Name the blood parasite species.
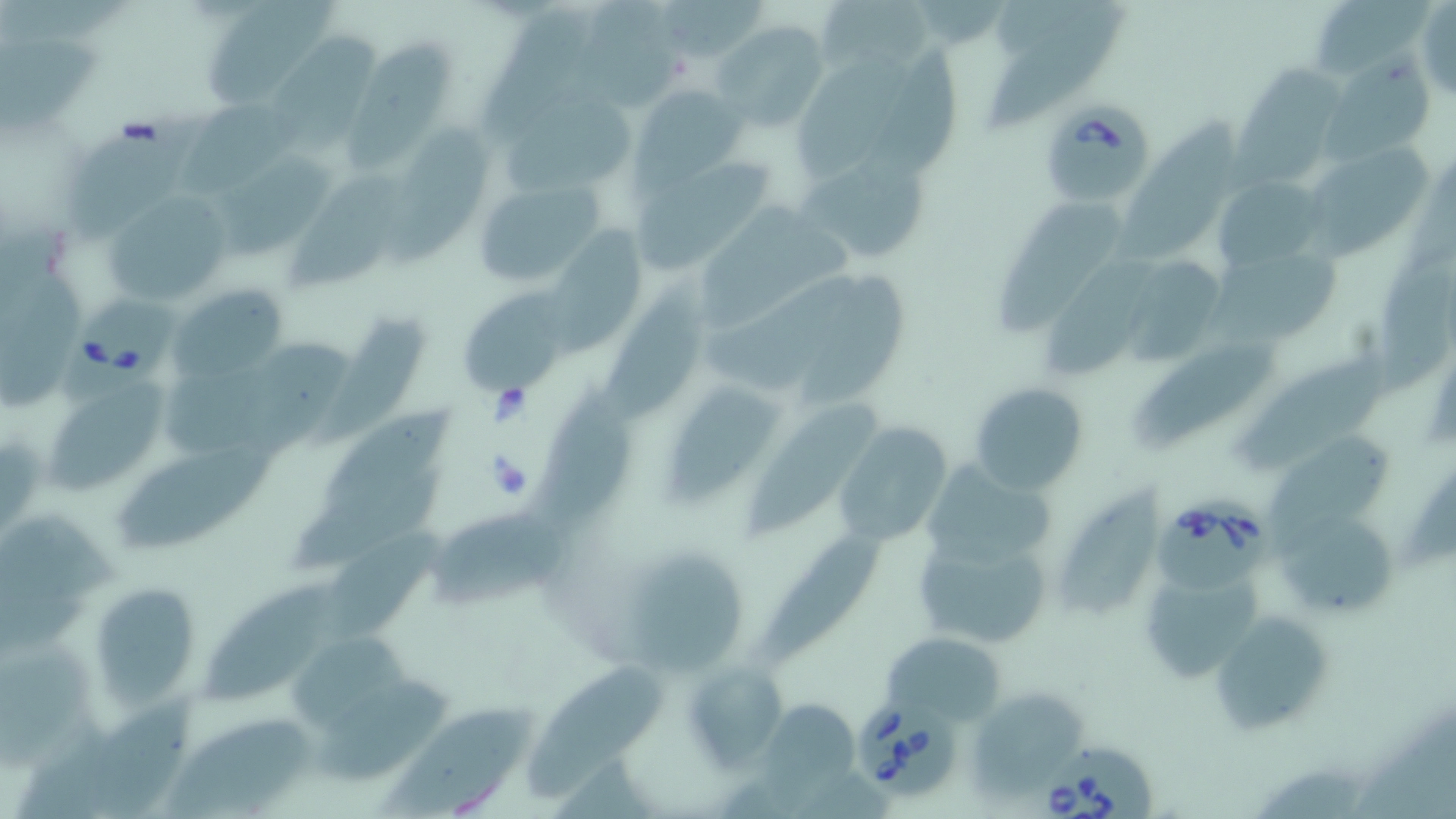
Babesia divergens.

Summary:
  - Coordinate format: approximate bounding boxes as (x1,y1)-(x2,y2) corner pairs in pixels
  - Uninfected red blood cell locations: (204,0)-(341,102), (659,0)-(764,65), (815,0)-(938,84), (914,0)-(999,43), (1314,0)-(1443,77), (575,1)-(689,110), (1415,4)-(1455,105), (478,5)-(597,144), (990,7)-(1129,131), (714,19)-(830,129), (265,27)-(380,158), (350,32)-(456,171), (3,33)-(102,131), (866,49)-(958,183), (795,55)-(919,184), (1319,56)-(1431,162), (1231,68)-(1351,200), (630,86)-(744,188), (506,87)-(632,197), (183,94)-(306,196), (66,106)-(203,240), (390,119)-(493,265), (1122,120)-(1241,265), (1307,142)-(1436,261), (204,146)-(339,260), (797,146)-(927,267), (635,154)-(778,272), (292,168)-(410,291), (1213,176)-(1326,276), (474,177)-(605,286), (1005,186)-(1133,331), (104,194)-(236,304), (695,198)-(858,333), (540,227)-(649,364), (1050,256)-(1152,383), (1379,256)-(1456,402), (1205,257)-(1344,354), (1132,262)-(1222,363), (1,270)-(80,408), (605,274)-(703,425), (804,275)-(914,409), (703,276)-(858,396), (169,278)-(288,384), (457,286)-(573,397), (313,302)-(438,456), (241,334)-(350,454), (1141,337)-(1279,452), (1252,347)-(1387,472), (166,360)-(289,458), (666,378)-(788,502), (49,379)-(178,494), (970,382)-(1089,495), (537,384)-(630,532), (751,402)-(892,536), (321,403)-(463,512), (836,420)-(952,546), (1268,435)-(1395,562), (112,439)-(274,548), (921,462)-(1059,573), (294,476)-(442,576), (1047,486)-(1170,624), (1274,504)-(1402,625), (426,508)-(576,611), (0,514)-(133,595), (763,525)-(893,666), (912,529)-(1056,651), (337,533)-(446,640), (617,544)-(747,677), (1138,561)-(1263,685), (94,579)-(196,711), (205,582)-(349,700), (1207,610)-(1331,736), (881,631)-(1005,727), (292,633)-(422,732), (4,636)-(103,771), (525,655)-(661,795), (681,659)-(787,773), (314,680)-(459,785), (971,686)-(1090,793), (93,689)-(199,819), (384,698)-(553,819), (768,700)-(859,811), (173,713)-(313,819), (21,731)-(119,819), (1257,766)-(1374,819)
  - Babesia divergens-infected red blood cell locations: (1050,99)-(1151,205), (60,287)-(181,405), (1157,490)-(1278,593), (850,693)-(959,794), (1042,737)-(1163,819)
  - Magnification: 1000x
  - Preparation: thin blood film
  - Stain: May-Grünwald-Giemsa
  - Image size: 1456×819 pixels
  - Field of view: one of a larger specimen
  - Modality: light microscopy